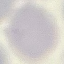

Malaria status: uninfected. Automatically extracted cell patch, resized to 64 × 64 pixels. Giemsa-stained preparation. Photographed with a smartphone camera at the microscope eyepiece. Thin blood smear.